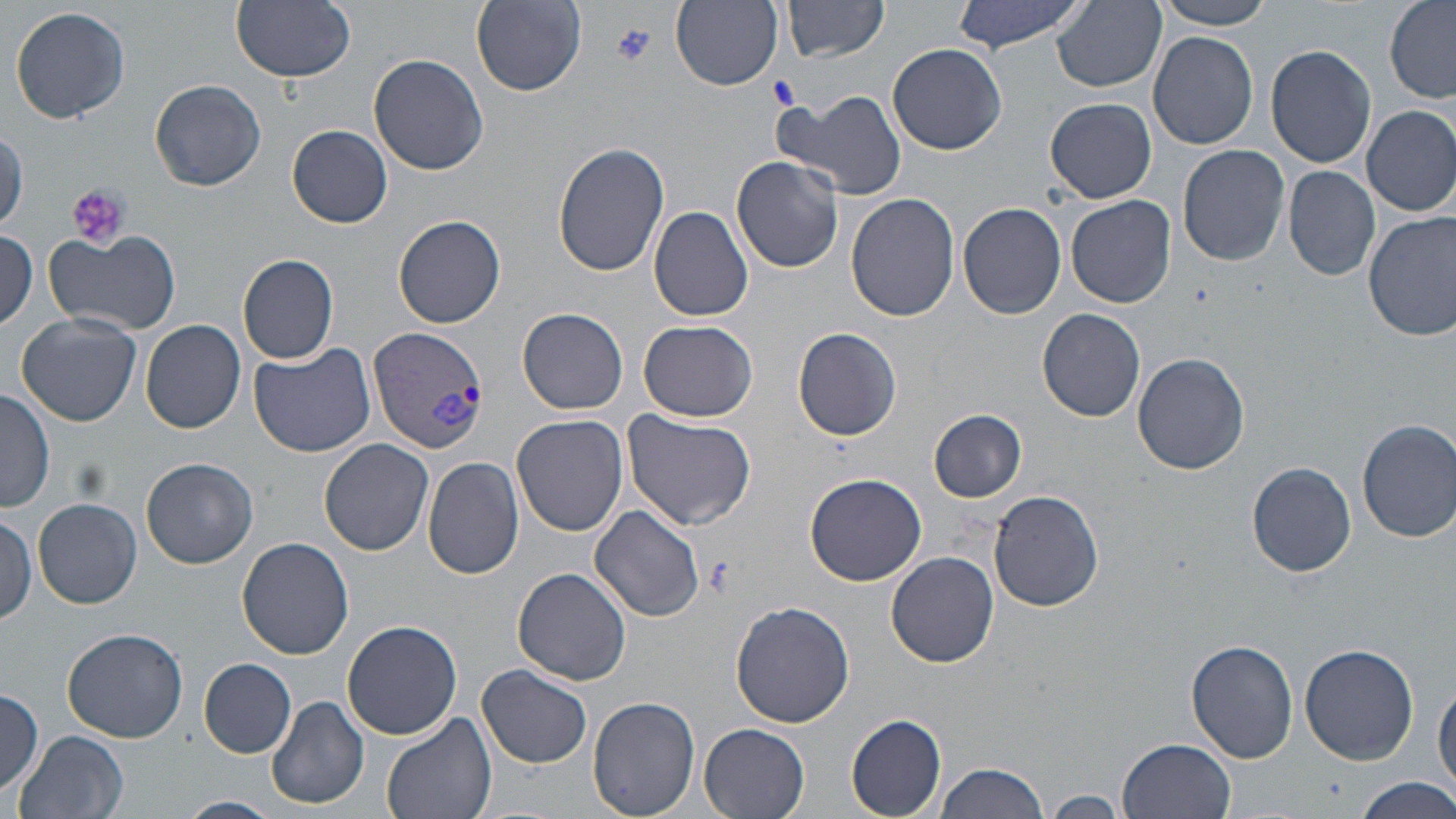
Approximate bounding boxes as [x1, y1, x2, y2] in pixels. Plasmodium vivax-infected red blood cell locations: [366, 326, 487, 456]. Uninfected red blood cell locations: [232, 0, 355, 82], [472, 0, 587, 95], [950, 0, 1092, 55], [1156, 0, 1274, 30], [1383, 0, 1456, 103], [671, 1, 785, 90], [784, 1, 887, 61], [1054, 1, 1168, 92], [9, 5, 132, 124], [1149, 30, 1258, 151], [887, 42, 1008, 155], [1266, 44, 1377, 169], [370, 52, 490, 174], [150, 79, 266, 192], [778, 88, 909, 202], [1045, 97, 1157, 203], [1361, 105, 1456, 217], [289, 124, 392, 228], [0, 131, 27, 232], [555, 142, 670, 277], [1177, 144, 1290, 266], [731, 156, 843, 273], [1283, 165, 1380, 281], [846, 193, 959, 322], [1065, 195, 1176, 308], [957, 203, 1066, 319], [648, 206, 754, 322], [1365, 210, 1456, 340], [393, 215, 506, 328], [0, 229, 39, 330], [44, 229, 183, 337], [238, 254, 340, 364], [518, 308, 628, 414], [1037, 308, 1147, 423], [16, 311, 145, 425], [638, 319, 759, 421], [141, 320, 246, 434], [792, 327, 902, 440], [249, 343, 376, 458], [1133, 351, 1250, 475], [0, 389, 54, 515], [929, 409, 1027, 502], [622, 411, 758, 532], [512, 414, 629, 537], [1357, 418, 1456, 542], [320, 438, 433, 555], [421, 456, 525, 581], [141, 457, 258, 568], [1247, 461, 1356, 577], [806, 472, 926, 584], [989, 489, 1104, 611], [33, 499, 142, 609], [589, 504, 704, 621], [0, 512, 39, 625], [237, 538, 354, 660], [886, 552, 999, 667], [512, 568, 631, 685], [732, 601, 854, 727], [343, 619, 463, 739], [63, 627, 187, 742], [1185, 639, 1299, 764], [1298, 642, 1419, 765], [200, 658, 297, 758], [477, 662, 593, 768], [1433, 678, 1456, 795], [0, 688, 44, 796], [265, 694, 369, 809], [588, 697, 701, 819], [380, 711, 497, 819], [846, 713, 949, 817], [698, 721, 810, 818], [15, 729, 130, 819], [1118, 738, 1236, 818], [933, 759, 1054, 819], [1353, 776, 1456, 818], [1046, 791, 1126, 817], [177, 795, 282, 818]. Platelet locations: [611, 22, 657, 66], [769, 76, 800, 109], [66, 184, 129, 251], [702, 558, 737, 597]. Slide-level diagnosis: Plasmodium vivax. Image is 1456×819 pixels. Captured at 1000x magnification. Optical microscopy. Single field of view. May-Grünwald-Giemsa-stained preparation. Thin blood smear.